Give the position of every Plasmodium parasite.
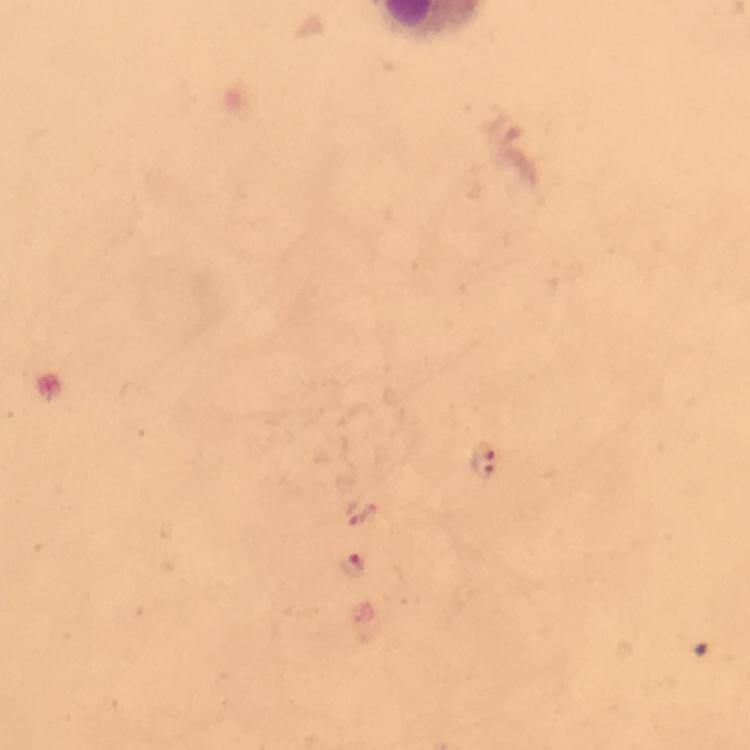
Approximate centers as (x, y) in pixels.
Plasmodium parasites: (485, 459), (363, 513), (355, 565).

cropped_from: one field of view
image_size: 750×750 pixels
preparation: thick blood film
stain: Giemsa
capture: smartphone photograph through a microscope
context: from a diagnostic examination for malaria
immersion_oil: applied
magnification: 100x